Give the extent of all Plasmodium falciparum-infected red blood cells.
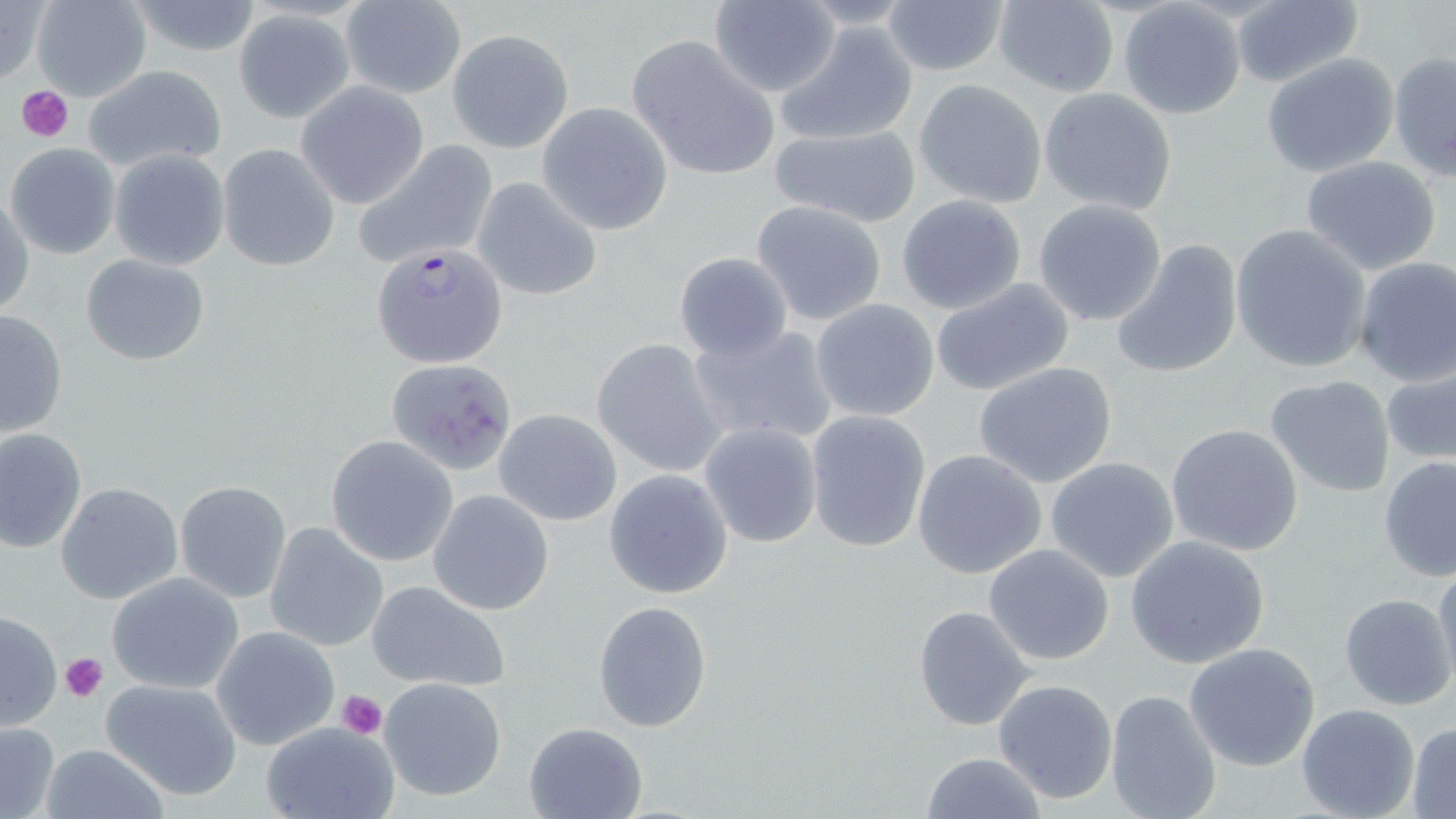
Approximate bounding boxes as [x1, y1, x2, y2] in pixels.
Plasmodium falciparum-infected red blood cells: [371, 242, 510, 369].

slide-level diagnosis = Plasmodium falciparum
field of view = single
platelet locations = approximate bounding boxes as [x1, y1, x2, y2] in pixels: [16, 85, 72, 141], [60, 654, 108, 702], [336, 689, 387, 739]
uninfected red blood cell locations = approximate bounding boxes as [x1, y1, x2, y2] in pixels: [31, 0, 153, 102], [992, 0, 1119, 97], [0, 1, 51, 86], [125, 1, 268, 58], [339, 1, 468, 99], [707, 1, 841, 98], [879, 1, 1011, 76], [1120, 2, 1246, 120], [1231, 2, 1364, 87], [233, 9, 356, 123], [775, 21, 921, 147], [447, 30, 574, 153], [627, 36, 780, 181], [1388, 51, 1456, 180], [1262, 55, 1399, 177], [81, 64, 229, 175], [914, 79, 1047, 208], [295, 81, 432, 210], [1039, 87, 1178, 215], [538, 104, 672, 235], [768, 123, 923, 229], [6, 142, 121, 259], [352, 142, 497, 270], [217, 144, 341, 271], [109, 148, 230, 272], [1299, 156, 1442, 274], [471, 177, 602, 302], [0, 192, 34, 320], [896, 193, 1026, 314], [1032, 199, 1167, 327], [752, 201, 887, 325], [1230, 223, 1372, 374], [1111, 239, 1243, 379], [673, 252, 794, 363], [80, 254, 211, 366], [1351, 257, 1456, 386], [930, 277, 1076, 396], [811, 298, 940, 422], [0, 307, 70, 439], [687, 323, 840, 449], [591, 338, 726, 477], [385, 357, 518, 475], [973, 362, 1118, 489], [1381, 366, 1456, 468], [1264, 374, 1397, 498], [493, 408, 623, 526], [805, 409, 930, 552], [697, 422, 822, 549], [1165, 423, 1305, 557], [0, 428, 87, 553], [325, 435, 458, 566], [912, 449, 1048, 580], [1045, 456, 1178, 581], [1378, 456, 1456, 581], [604, 470, 733, 599], [176, 481, 292, 601], [56, 482, 184, 605], [427, 490, 555, 615], [265, 520, 389, 653], [1125, 535, 1272, 670], [983, 544, 1114, 665], [1429, 561, 1456, 692], [106, 573, 244, 694], [365, 581, 512, 693], [1339, 593, 1454, 710], [594, 602, 711, 731], [913, 605, 1034, 730], [0, 611, 62, 731], [212, 626, 342, 750], [1183, 641, 1322, 771], [378, 676, 508, 802], [100, 677, 243, 799], [992, 679, 1120, 804], [1103, 689, 1223, 819], [1297, 703, 1420, 819], [524, 721, 648, 819], [0, 722, 60, 817], [1407, 722, 1456, 818], [263, 724, 398, 819], [40, 742, 170, 818], [920, 752, 1048, 819]
magnification = 1000x
image size = 1456×819 pixels
preparation = thin blood smear
stain = May-Grünwald-Giemsa
modality = optical microscopy